Assess this cell for malaria.
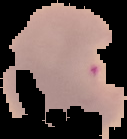

Parasitized.

Summary:
  - Image type: segmented cell region with the area outside set to black
  - Image size: 127×139 pixels
  - Preparation: thin blood film